Locate every blood parasite and identify its species.
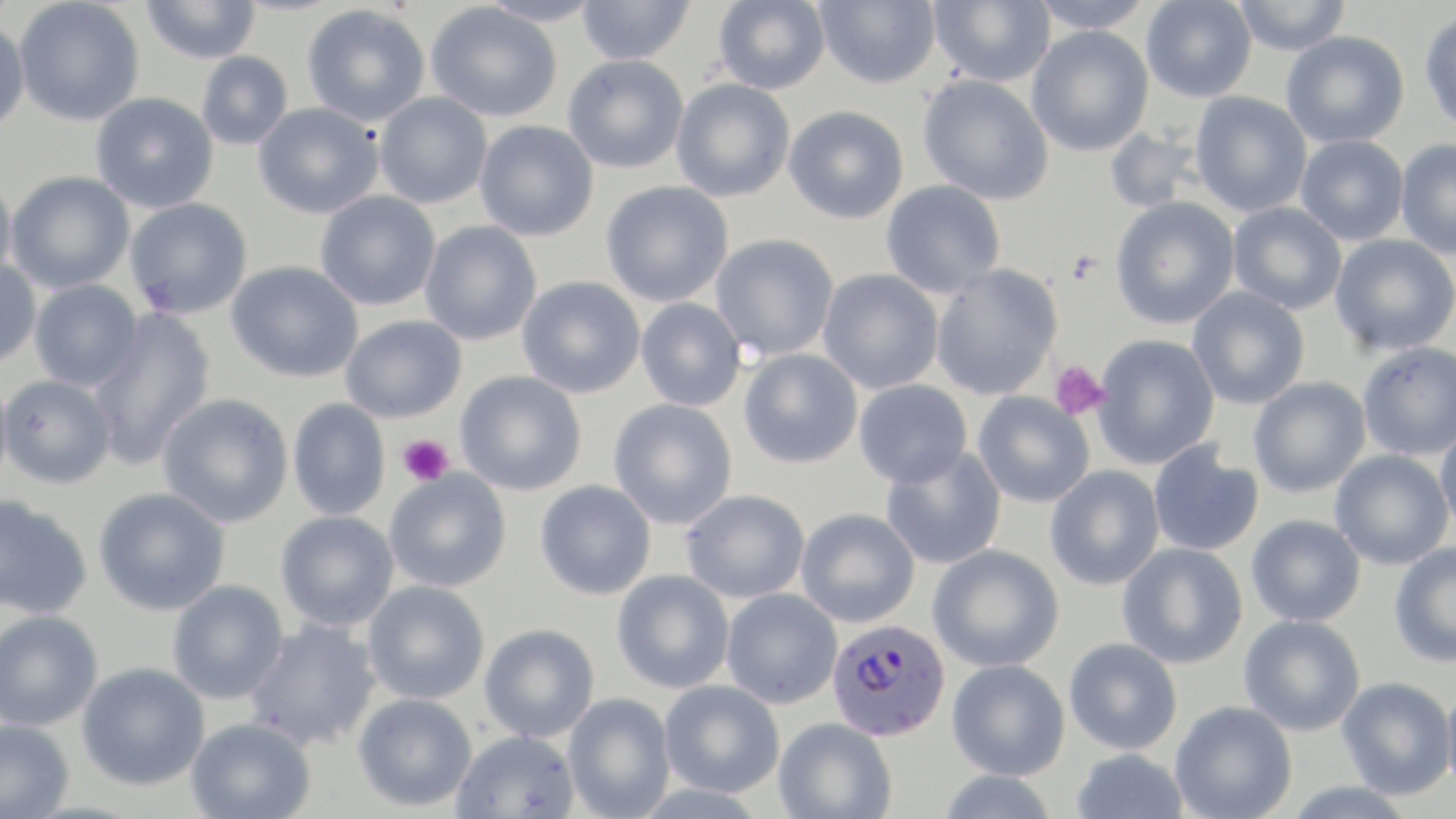
Approximate bounding boxes as named x1/y1/x2/y2 corners in pixels.
Plasmodium falciparum-infected red blood cells: (x1=826, y1=619, x2=951, y2=742).
No Plasmodium ovale, Plasmodium malariae, Plasmodium vivax, Babesia divergens, or Trypanosoma brucei observed.

slide_level_diagnosis: Plasmodium falciparum
modality: optical microscopy
field_of_view: one of a larger specimen
preparation: thin blood film
image_size: 1456×819 pixels
platelet_locations: 'approximate bounding boxes as named x1/y1/x2/y2 corners in pixels: (x1=1049, y1=360, x2=1108, y2=420), (x1=398, y1=434, x2=454, y2=485)'
uninfected_red_blood_cell_locations: 'approximate bounding boxes as named x1/y1/x2/y2 corners in pixels: (x1=14, y1=0, x2=144, y2=126), (x1=478, y1=0, x2=603, y2=27), (x1=577, y1=0, x2=694, y2=65), (x1=713, y1=0, x2=831, y2=94), (x1=815, y1=0, x2=941, y2=89), (x1=929, y1=0, x2=1055, y2=87), (x1=1029, y1=0, x2=1154, y2=34), (x1=1141, y1=0, x2=1257, y2=102), (x1=1231, y1=0, x2=1352, y2=56), (x1=140, y1=1, x2=261, y2=64), (x1=426, y1=2, x2=562, y2=123), (x1=302, y1=4, x2=430, y2=127), (x1=1419, y1=10, x2=1456, y2=135), (x1=0, y1=18, x2=30, y2=134), (x1=1026, y1=26, x2=1154, y2=157), (x1=1281, y1=31, x2=1410, y2=148), (x1=196, y1=51, x2=292, y2=150), (x1=563, y1=54, x2=688, y2=174), (x1=918, y1=74, x2=1054, y2=206), (x1=671, y1=78, x2=795, y2=203), (x1=91, y1=92, x2=218, y2=214), (x1=374, y1=92, x2=492, y2=209), (x1=1190, y1=92, x2=1312, y2=217), (x1=253, y1=102, x2=384, y2=219), (x1=784, y1=106, x2=909, y2=224), (x1=474, y1=120, x2=598, y2=242), (x1=1104, y1=127, x2=1203, y2=214), (x1=1295, y1=135, x2=1409, y2=245), (x1=1394, y1=139, x2=1456, y2=259), (x1=5, y1=171, x2=134, y2=293), (x1=0, y1=173, x2=17, y2=288), (x1=880, y1=180, x2=1005, y2=298), (x1=600, y1=181, x2=733, y2=307), (x1=315, y1=191, x2=440, y2=311), (x1=1110, y1=197, x2=1240, y2=329), (x1=125, y1=198, x2=253, y2=319), (x1=1228, y1=202, x2=1347, y2=314), (x1=420, y1=221, x2=542, y2=346), (x1=711, y1=233, x2=839, y2=361), (x1=1330, y1=234, x2=1456, y2=356), (x1=0, y1=259, x2=42, y2=368), (x1=226, y1=261, x2=364, y2=383), (x1=930, y1=263, x2=1063, y2=401), (x1=818, y1=269, x2=944, y2=394), (x1=517, y1=275, x2=645, y2=399), (x1=29, y1=280, x2=143, y2=391), (x1=1187, y1=287, x2=1310, y2=410), (x1=636, y1=297, x2=747, y2=412), (x1=87, y1=309, x2=216, y2=469), (x1=341, y1=315, x2=467, y2=423), (x1=1091, y1=334, x2=1220, y2=470), (x1=1357, y1=342, x2=1456, y2=460), (x1=738, y1=349, x2=863, y2=469), (x1=0, y1=368, x2=13, y2=493), (x1=456, y1=371, x2=587, y2=496), (x1=1, y1=374, x2=115, y2=488), (x1=1248, y1=377, x2=1371, y2=498), (x1=853, y1=379, x2=972, y2=488), (x1=972, y1=391, x2=1095, y2=508), (x1=157, y1=393, x2=294, y2=528), (x1=287, y1=398, x2=390, y2=520), (x1=608, y1=399, x2=738, y2=530), (x1=1434, y1=421, x2=1456, y2=535), (x1=1148, y1=442, x2=1264, y2=557), (x1=880, y1=445, x2=1007, y2=570), (x1=1331, y1=450, x2=1453, y2=570), (x1=1044, y1=465, x2=1165, y2=591), (x1=384, y1=469, x2=512, y2=593), (x1=535, y1=480, x2=656, y2=600), (x1=93, y1=487, x2=230, y2=616), (x1=680, y1=489, x2=810, y2=603), (x1=0, y1=494, x2=92, y2=620), (x1=796, y1=508, x2=920, y2=627), (x1=275, y1=510, x2=399, y2=631), (x1=1246, y1=514, x2=1366, y2=627), (x1=1117, y1=542, x2=1248, y2=668), (x1=1388, y1=542, x2=1456, y2=668), (x1=927, y1=544, x2=1064, y2=672), (x1=611, y1=569, x2=734, y2=694), (x1=167, y1=580, x2=288, y2=704), (x1=362, y1=580, x2=490, y2=704), (x1=721, y1=588, x2=842, y2=709), (x1=0, y1=609, x2=103, y2=731), (x1=1238, y1=615, x2=1366, y2=736), (x1=244, y1=619, x2=382, y2=751), (x1=479, y1=623, x2=599, y2=742), (x1=1063, y1=638, x2=1183, y2=754), (x1=947, y1=659, x2=1070, y2=780), (x1=77, y1=662, x2=209, y2=791), (x1=1336, y1=676, x2=1455, y2=800), (x1=1441, y1=677, x2=1456, y2=803), (x1=659, y1=679, x2=784, y2=797), (x1=353, y1=692, x2=477, y2=811), (x1=563, y1=693, x2=676, y2=819), (x1=1169, y1=701, x2=1297, y2=819), (x1=185, y1=717, x2=316, y2=818), (x1=773, y1=717, x2=897, y2=819), (x1=0, y1=718, x2=75, y2=819), (x1=452, y1=729, x2=580, y2=819), (x1=1071, y1=748, x2=1190, y2=819), (x1=935, y1=770, x2=1060, y2=819), (x1=1282, y1=782, x2=1415, y2=818)'
magnification: 1000x
stain: May-Grünwald-Giemsa